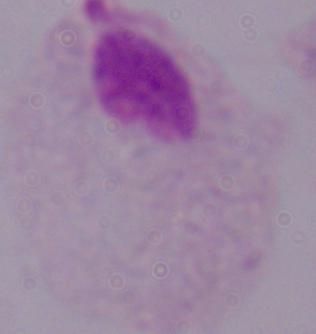
Micrograph. A trichomonad is shown. 1000x magnification.